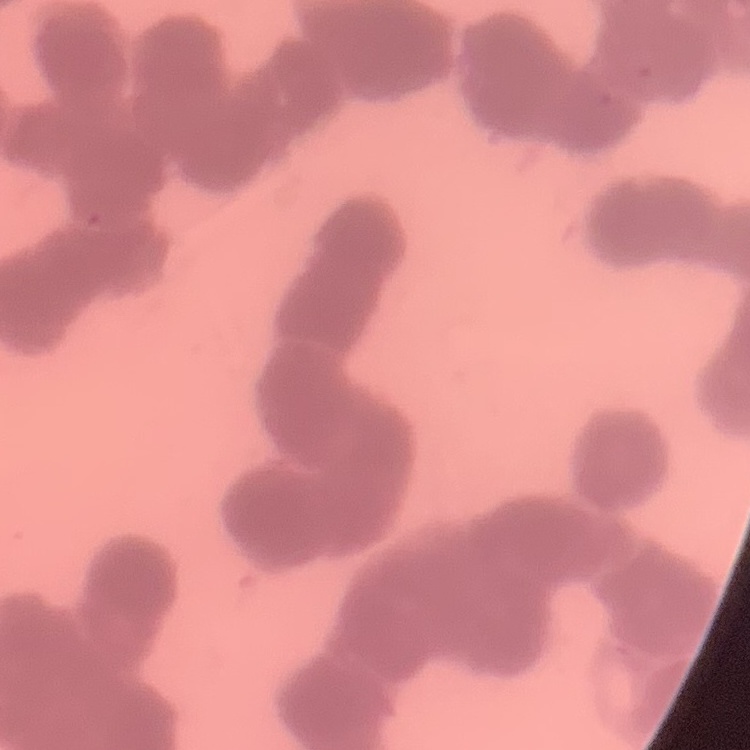
Summary:
  - Red blood cell morphology: rouleaux formation
  - Stain: Field's or Giemsa
  - Preparation: thin blood film
  - Image type: square crop of a larger photomicrograph